Assess this cell for malaria.
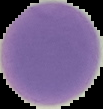

Uninfected.

Cell region segmented out of the field of view; the surrounding area is masked to black. From a thin blood film. Image is 103×109 pixels.